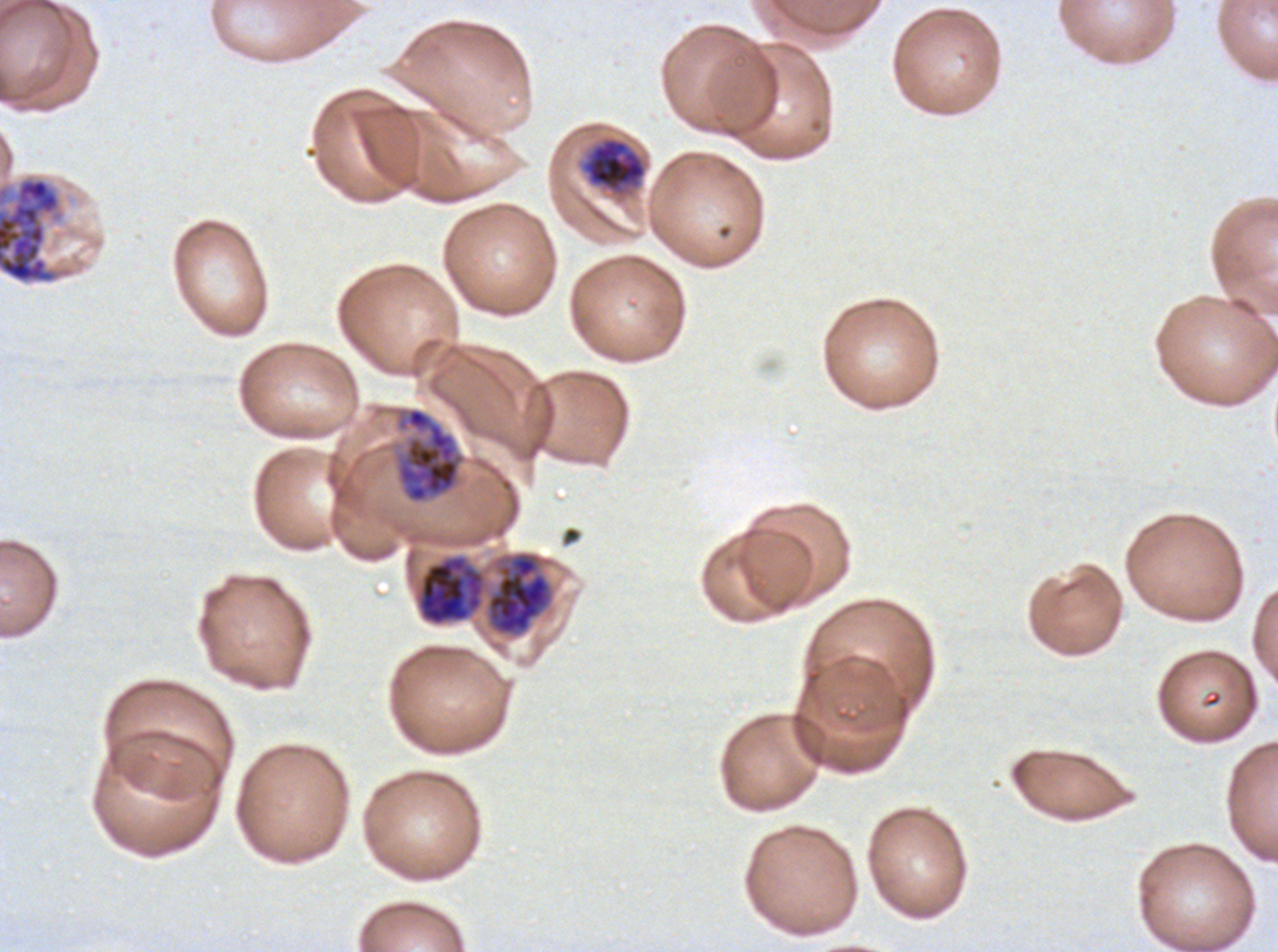
notation = approximate bounding boxes as [x1, y1, x2, y2] in pixels
late trophozoite locations = [582, 137, 646, 193]
early schizont locations = [395, 406, 466, 505]
late schizont locations = [0, 176, 73, 285], [485, 551, 553, 636], [417, 555, 485, 625]
field of view = one sub-image of a larger composite
preparation = thin blood smear
life-cycle stages observed = late trophozoite, early schizont, late schizont
specimen = ex-vivo Plasmodium falciparum culture from a patient in The Gambia, grown for 24 to 48 hours
image size = 1278×952 pixels
stain = Giemsa